Comment on the morphology of the red blood cells.
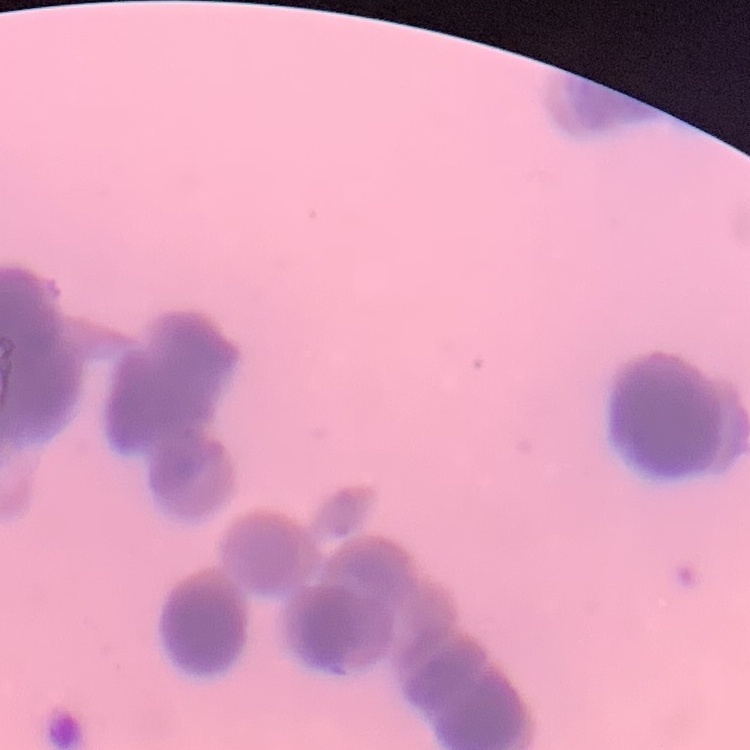
Rouleaux formation.

Thin peripheral smear. Stained with either Field's or Giemsa. One tile cut from a larger photomicrograph.